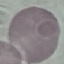
Summary:
  - Result: no malaria parasites seen
  - Preparation: thin smear
  - Capture: smartphone through the microscope eyepiece
  - Image type: automatically extracted cell patch, resized to 64 × 64 pixels
  - Stain: Giemsa